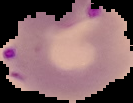

Summary:
  - Preparation: thin blood film
  - Image size: 133×103 pixels
  - Malaria status: parasitized
  - Image type: segmented cell region on a black background